Report the malaria status of this cell.
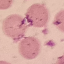
Uninfected.

preparation = thin blood film
capture = smartphone through the microscope eyepiece
image type = cell patch, automatically extracted from a larger field of view and resized to 64 × 64 pixels
stain = Giemsa